Assess this cell for malaria.
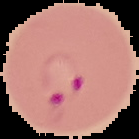

Parasitized.

Summary:
  - Preparation: thin blood smear
  - Image type: cell region segmented out of the field of view; surrounding area masked to black
  - Image size: 139×139 pixels